Name the parasite shown.
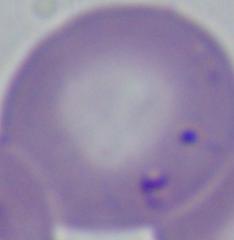

This is Babesia.

magnification = 1000x
modality = micrograph